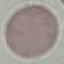

Summary:
  - Result: no malaria parasites seen
  - Preparation: thin smear
  - Capture: smartphone camera at the microscope eyepiece
  - Image type: cell patch, automatically extracted from a larger field of view and resized to 64 × 64 pixels
  - Stain: Giemsa